State the blood parasite species.
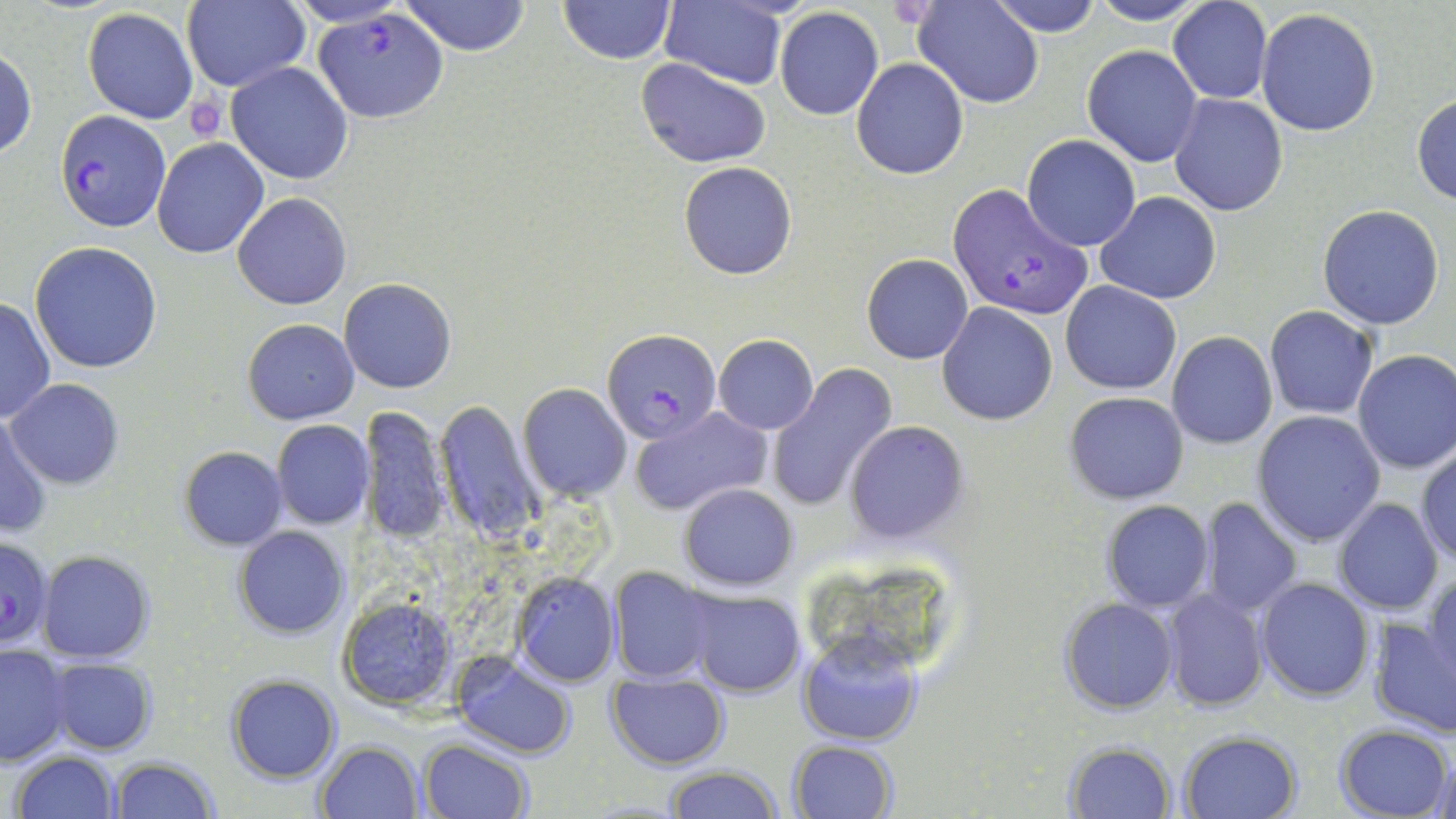

Plasmodium falciparum.

Summary:
  - Coordinate format: approximate bounding boxes as (x1, y1, x2, y2) in pixels
  - Plasmodium falciparum-infected red blood cell locations: (313, 10, 448, 124), (56, 109, 170, 232), (947, 181, 1092, 324), (603, 329, 720, 440), (0, 535, 55, 650)
  - Uninfected red blood cell locations: (182, 0, 310, 93), (286, 0, 409, 28), (402, 0, 530, 55), (558, 0, 675, 65), (657, 0, 790, 90), (913, 0, 1044, 108), (985, 0, 1104, 36), (1086, 0, 1212, 25), (1169, 1, 1272, 103), (774, 7, 884, 121), (81, 8, 199, 124), (1256, 8, 1381, 136), (1082, 45, 1203, 167), (0, 49, 36, 160), (852, 58, 969, 179), (637, 59, 770, 168), (226, 62, 353, 185), (1168, 93, 1287, 216), (1412, 93, 1456, 205), (1023, 134, 1141, 251), (152, 139, 269, 258), (678, 162, 798, 279), (233, 192, 351, 309), (1095, 192, 1222, 305), (1317, 204, 1445, 330), (31, 242, 164, 374), (861, 253, 973, 364), (338, 278, 457, 393), (1060, 280, 1181, 395), (0, 297, 54, 424), (939, 303, 1056, 425), (1264, 305, 1379, 419), (243, 319, 360, 423), (1167, 331, 1277, 450), (713, 335, 819, 435), (1353, 349, 1456, 474), (767, 366, 896, 510), (8, 378, 124, 490), (518, 384, 632, 501), (1065, 392, 1188, 503), (434, 400, 543, 544), (359, 404, 452, 544), (629, 405, 772, 517), (0, 410, 51, 540), (1251, 410, 1386, 545), (845, 420, 968, 545), (271, 421, 375, 530), (179, 445, 287, 549), (1415, 446, 1456, 566), (678, 483, 800, 590), (1200, 497, 1302, 615), (1335, 499, 1444, 617), (1101, 501, 1214, 612), (234, 526, 348, 638), (37, 550, 155, 662), (608, 567, 719, 683), (510, 571, 620, 685), (1424, 572, 1456, 688), (1256, 577, 1373, 701), (684, 587, 807, 698), (1160, 590, 1270, 710), (339, 595, 457, 709), (1058, 596, 1179, 714), (1369, 613, 1455, 739), (798, 631, 921, 748), (0, 645, 74, 764), (449, 651, 578, 759), (44, 656, 157, 754), (605, 673, 729, 769), (225, 674, 342, 784), (1334, 724, 1453, 818), (1178, 730, 1303, 819), (788, 738, 898, 818), (1062, 738, 1178, 817), (316, 739, 424, 819), (420, 739, 533, 819), (13, 750, 121, 818), (1426, 750, 1454, 817), (109, 756, 219, 819), (664, 764, 784, 819)
  - Platelet locations: (185, 95, 227, 140)
  - Magnification: 1000x
  - Image size: 1456×819 pixels
  - Field of view: one of a larger specimen
  - Preparation: thin blood film
  - Modality: optical microscopy
  - Stain: May-Grünwald-Giemsa